Locate every blood parasite and identify its species.
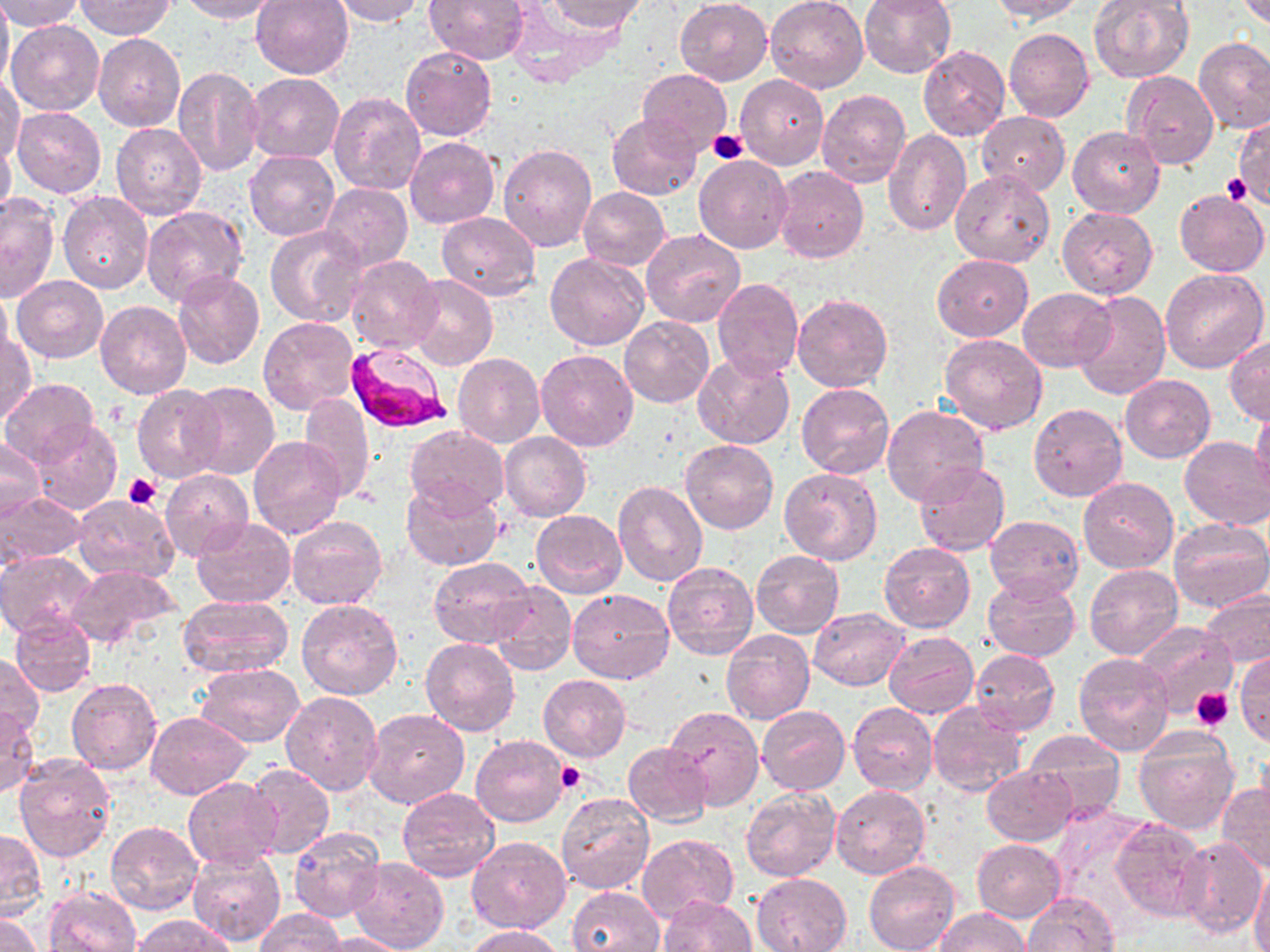

Approximate bounding boxes as (x1, y1, x2, y2) in pixels.
Plasmodium falciparum-infected red blood cells: (346, 341, 452, 435).
No Plasmodium ovale, Plasmodium malariae, Plasmodium vivax, Babesia divergens, or Trypanosoma brucei observed.

Uninfected red blood cell locations: (0, 0, 12, 93), (0, 0, 83, 31), (178, 0, 281, 23), (250, 0, 356, 79), (329, 0, 424, 25), (425, 0, 529, 64), (543, 0, 645, 34), (676, 0, 773, 85), (766, 0, 869, 93), (859, 0, 958, 78), (987, 0, 1087, 23), (1233, 0, 1270, 28), (75, 1, 176, 39), (1087, 1, 1194, 84), (7, 21, 105, 116), (1005, 28, 1094, 123), (93, 34, 186, 132), (1194, 37, 1270, 133), (400, 45, 496, 141), (918, 45, 1010, 140), (171, 64, 264, 175), (639, 69, 731, 152), (1123, 71, 1218, 171), (0, 72, 25, 166), (246, 73, 344, 162), (736, 74, 828, 169), (817, 89, 911, 188), (327, 92, 425, 197), (844, 101, 957, 214), (12, 106, 105, 199), (977, 111, 1070, 196), (607, 112, 701, 201), (1234, 116, 1270, 209), (111, 122, 206, 221), (1068, 126, 1164, 217), (883, 129, 970, 236), (0, 133, 16, 221), (405, 137, 500, 228), (497, 144, 596, 252), (244, 150, 339, 241), (694, 154, 792, 253), (772, 166, 868, 264), (950, 168, 1055, 268), (321, 183, 413, 270), (578, 186, 670, 270), (1174, 190, 1269, 277), (0, 192, 59, 302), (58, 192, 154, 294), (140, 206, 248, 306), (1056, 206, 1158, 298), (436, 211, 541, 301), (267, 225, 365, 327), (641, 229, 745, 329), (545, 251, 649, 350), (931, 254, 1033, 341), (345, 255, 442, 354), (1161, 270, 1269, 374), (173, 272, 265, 371), (408, 274, 497, 371), (13, 276, 108, 363), (712, 276, 804, 381), (1075, 281, 1258, 384), (1018, 287, 1115, 373), (0, 288, 13, 363), (1071, 289, 1170, 399), (793, 294, 893, 393), (95, 301, 192, 398), (619, 316, 713, 407), (259, 317, 359, 414), (1, 332, 36, 424), (940, 334, 1049, 436), (1226, 335, 1270, 426), (536, 349, 638, 451), (693, 352, 793, 450), (454, 354, 545, 448), (1121, 375, 1215, 462), (2, 378, 100, 469), (187, 383, 280, 481), (796, 383, 894, 479), (132, 385, 226, 483), (299, 394, 374, 499), (1029, 403, 1126, 501), (1252, 403, 1270, 498), (881, 406, 988, 507), (30, 418, 122, 514), (404, 425, 508, 517), (500, 432, 591, 522), (248, 436, 346, 539), (1179, 436, 1270, 530), (0, 437, 44, 523), (681, 440, 777, 534), (913, 462, 1010, 557), (778, 467, 883, 566), (160, 470, 254, 561), (1078, 477, 1178, 573), (613, 480, 708, 587), (402, 481, 504, 571), (0, 491, 87, 566), (72, 494, 179, 584), (531, 509, 626, 598), (288, 515, 388, 610), (985, 515, 1084, 603), (193, 516, 296, 609), (1167, 518, 1270, 613), (879, 542, 975, 632), (0, 550, 97, 639), (752, 551, 844, 636), (430, 557, 536, 649), (662, 562, 758, 660), (66, 563, 177, 649), (1084, 563, 1183, 659), (982, 578, 1080, 662), (489, 580, 577, 676), (567, 588, 674, 683), (1200, 588, 1270, 669), (178, 595, 291, 679), (297, 598, 402, 701), (809, 608, 909, 690), (9, 613, 96, 696), (1136, 621, 1236, 716), (721, 629, 815, 725), (884, 631, 979, 718), (422, 638, 520, 736), (968, 648, 1058, 737), (1235, 649, 1269, 747), (0, 653, 42, 739), (1072, 653, 1173, 756), (390, 657, 495, 774), (194, 663, 304, 747), (538, 674, 630, 762), (67, 678, 162, 775), (280, 691, 383, 795), (848, 704, 938, 795), (929, 704, 1026, 797), (663, 706, 764, 810), (0, 707, 38, 799), (363, 707, 470, 810), (757, 707, 850, 795), (146, 711, 251, 798), (1133, 726, 1241, 834), (1023, 731, 1127, 820), (470, 735, 569, 827), (623, 741, 713, 827), (13, 754, 117, 861), (245, 764, 334, 859), (982, 765, 1075, 845), (182, 778, 282, 868), (1218, 782, 1270, 873), (832, 784, 931, 879), (740, 786, 840, 882), (398, 787, 499, 882), (556, 794, 654, 894), (1047, 807, 1154, 921), (1109, 817, 1207, 923), (105, 821, 202, 915), (289, 826, 386, 924), (1, 829, 47, 917), (638, 833, 740, 921), (466, 836, 571, 932), (1176, 837, 1267, 938), (973, 838, 1065, 921), (186, 850, 285, 946), (349, 858, 448, 952), (864, 861, 958, 952), (1249, 869, 1270, 952), (752, 872, 852, 951), (42, 886, 140, 952), (566, 886, 663, 952), (1023, 892, 1119, 952), (659, 894, 755, 952), (934, 907, 1030, 952), (254, 908, 344, 951), (0, 911, 42, 952), (131, 915, 238, 952), (464, 925, 568, 952), (319, 931, 413, 951). Platelet locations: (1234, 124, 1267, 208), (707, 129, 749, 163), (1223, 174, 1249, 202), (123, 473, 163, 509), (1191, 687, 1234, 731), (555, 760, 584, 793). Slide-level diagnosis: Plasmodium falciparum. Thin blood film. Image is 1270×952 pixels. 1000x magnification. Light microscopy. One field of a larger specimen. May-Grünwald-Giemsa stain.